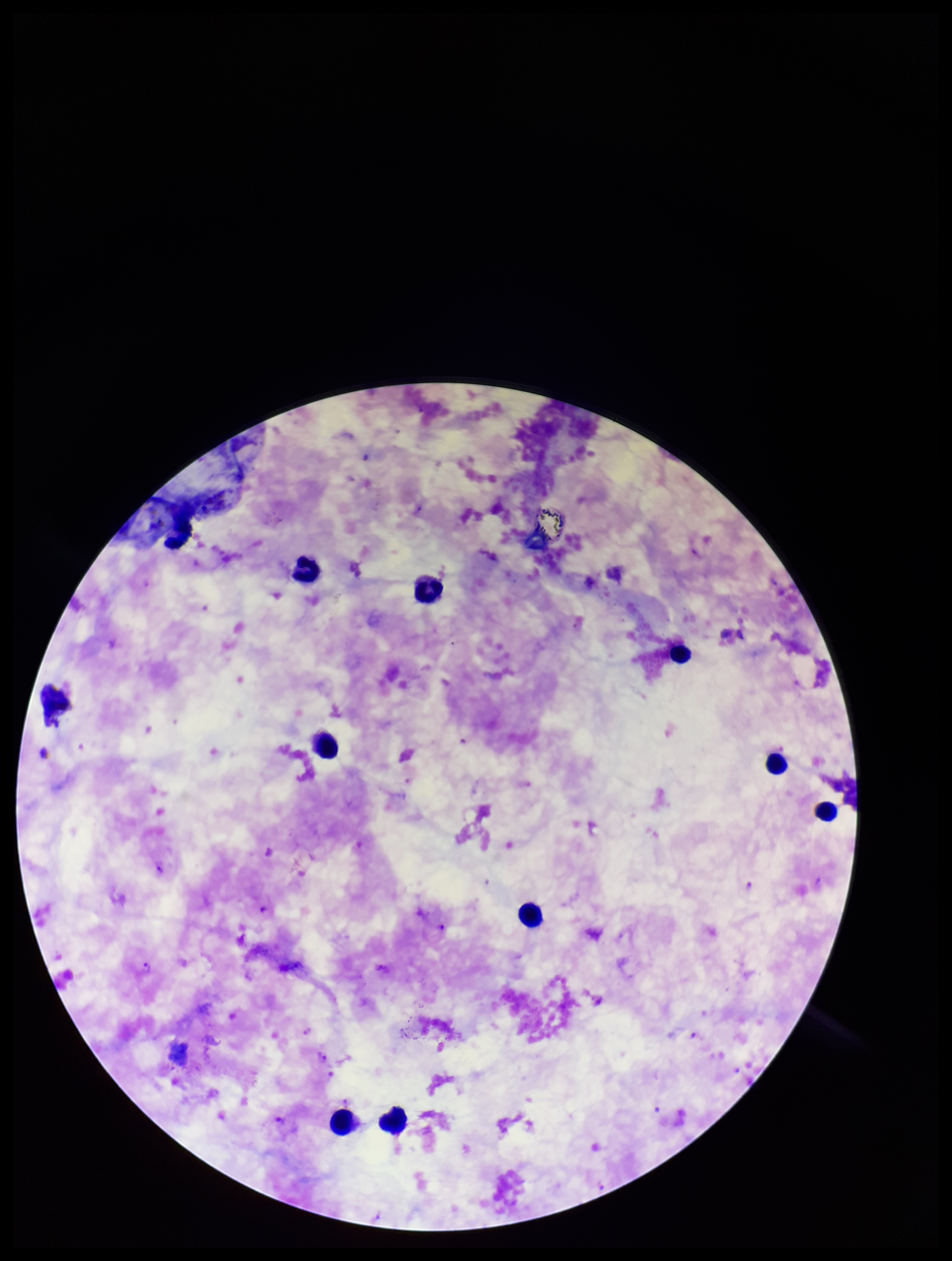
Summary:
  - Patient malaria status: positive
  - Leukocyte count: 9
  - Parasite count: 5
  - Field of view: single
  - Stain: Giemsa
  - Species reported for this patient: Plasmodium falciparum
  - Capture: smartphone photograph through the microscope eyepiece
  - Preparation: thick blood smear
  - Image size: 952×1261 pixels
  - Plasmodium parasites: identified